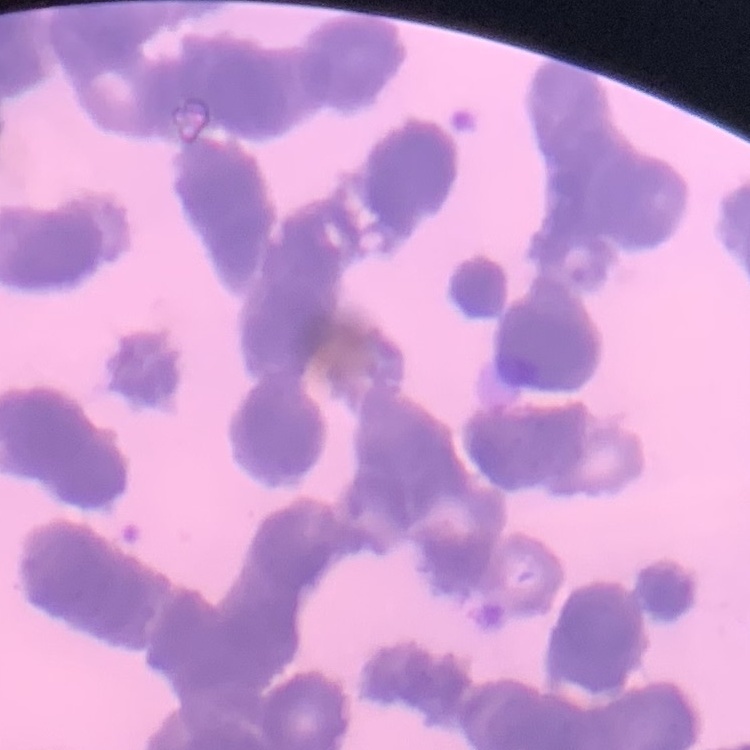

The red blood cells exhibit rouleaux formation. Square crop of a larger photomicrograph. Thin blood film. Field's or Giemsa stain.